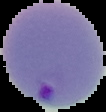

Image is 106×112 pixels. Cell region segmented out of the field of view; the surrounding area is masked to black. From a thin blood film. Malaria status: parasitized.